Assess this cell for malaria.
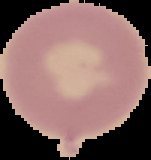

Uninfected.

Summary:
  - Image size: 151×160 pixels
  - Preparation: thin blood film
  - Image type: segmented cell region with the area outside set to black